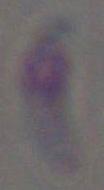

identification = Toxoplasma gondii
modality = photomicrograph
magnification = 1000x